Assess the morphology of the erythrocytes.
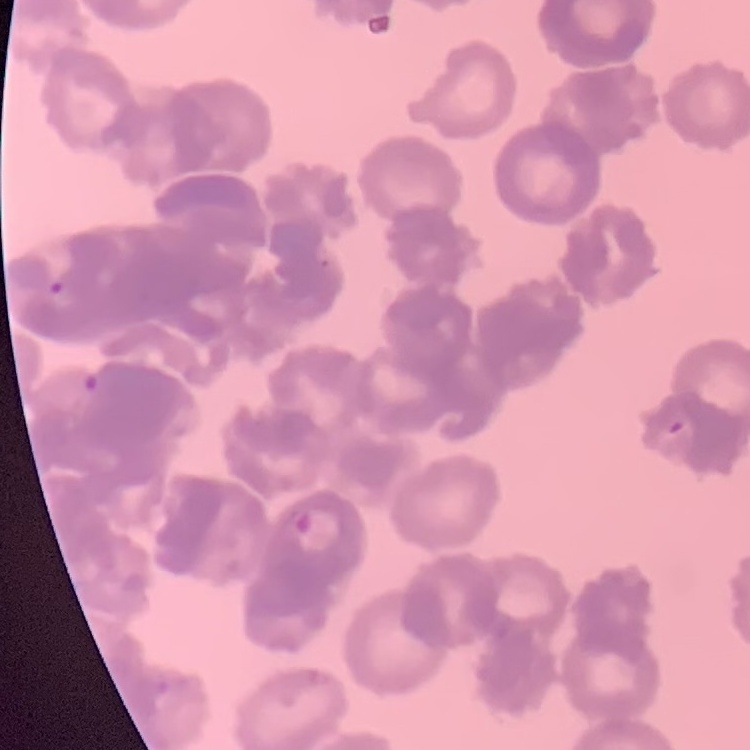

Rouleaux formation.

preparation = thin blood film
image type = square crop of a larger photomicrograph
stain = Field's or Giemsa